Report the malaria status of this cell.
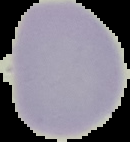
It is uninfected.

image size = 130×142 pixels
image type = segmented cell region with the area outside set to black
preparation = thin blood smear